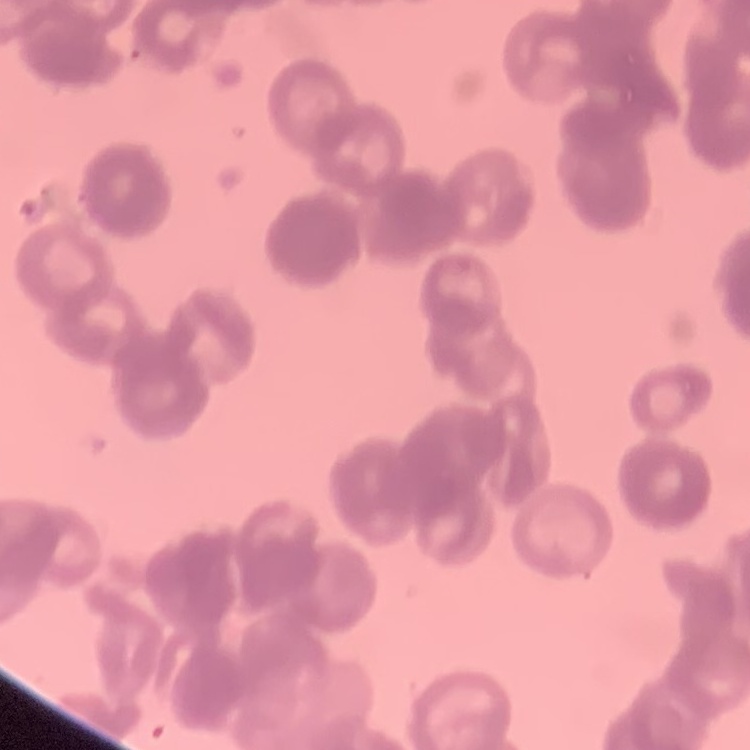

Summary:
  - Red blood cell morphology: rouleaux formation
  - Stain: Field's or Giemsa
  - Preparation: thin peripheral smear
  - Image type: one tile cut from a larger photomicrograph